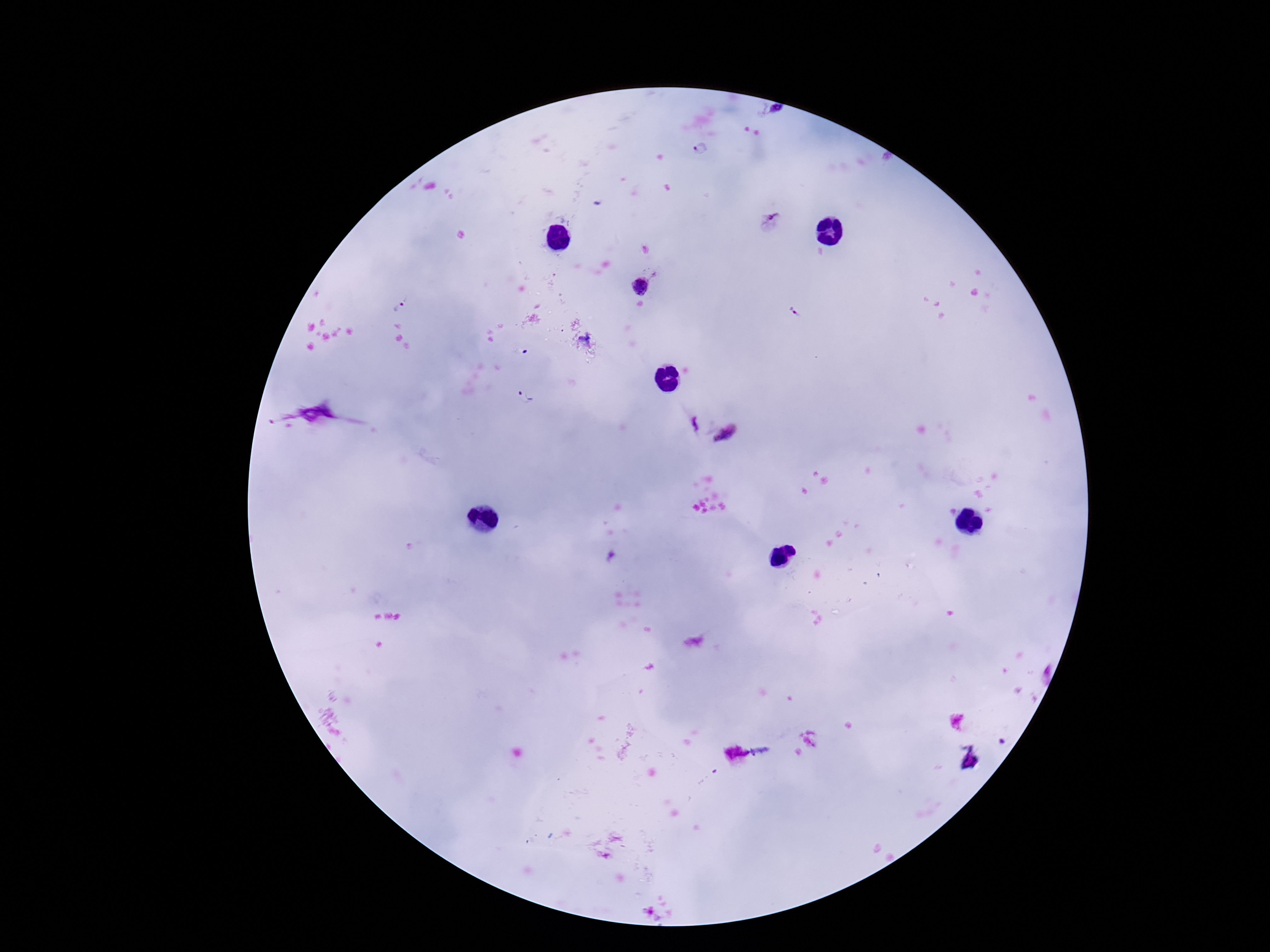

magnification = 100x
field of view = one from this slide
patient malaria status = positive
capture = smartphone camera through the microscope eyepiece
stain = Giemsa
image size = 1270×952 pixels
preparation = thick peripheral-blood smear
Plasmodium parasite locations = approximate centers as (x, y) in pixels: (775, 110), (701, 148), (771, 218), (654, 273), (641, 285), (401, 304), (585, 339), (526, 399), (696, 422), (729, 434)